Describe the morphology of the erythrocytes.
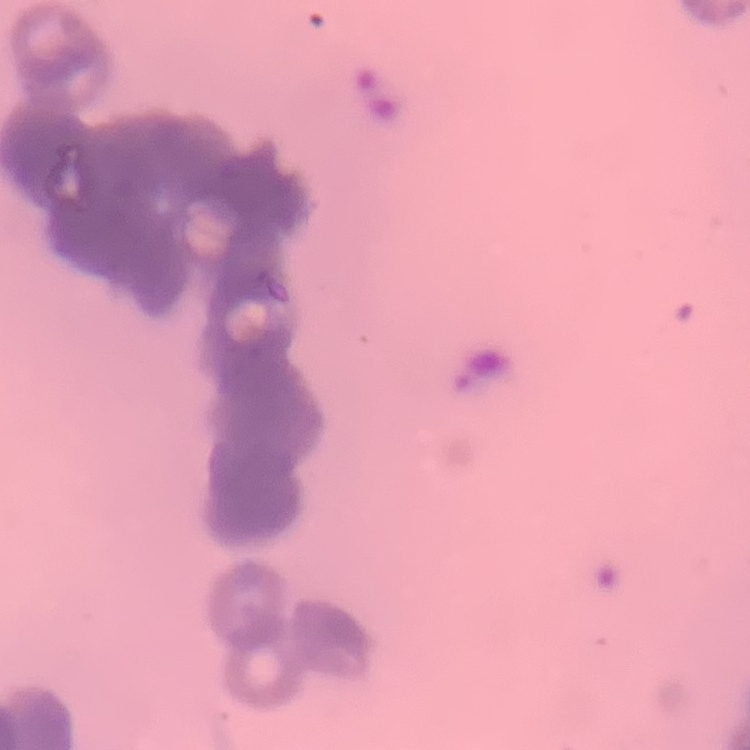
They show rouleaux formation.

{
  "stain": "Field's or Giemsa",
  "preparation": "thin blood film",
  "image_type": "one tile cut from a larger photomicrograph"
}